Assess this cell for malaria.
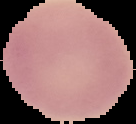
Uninfected.

Summary:
  - Image type: segmented cell region on a black background
  - Preparation: thin blood film
  - Image size: 136×124 pixels